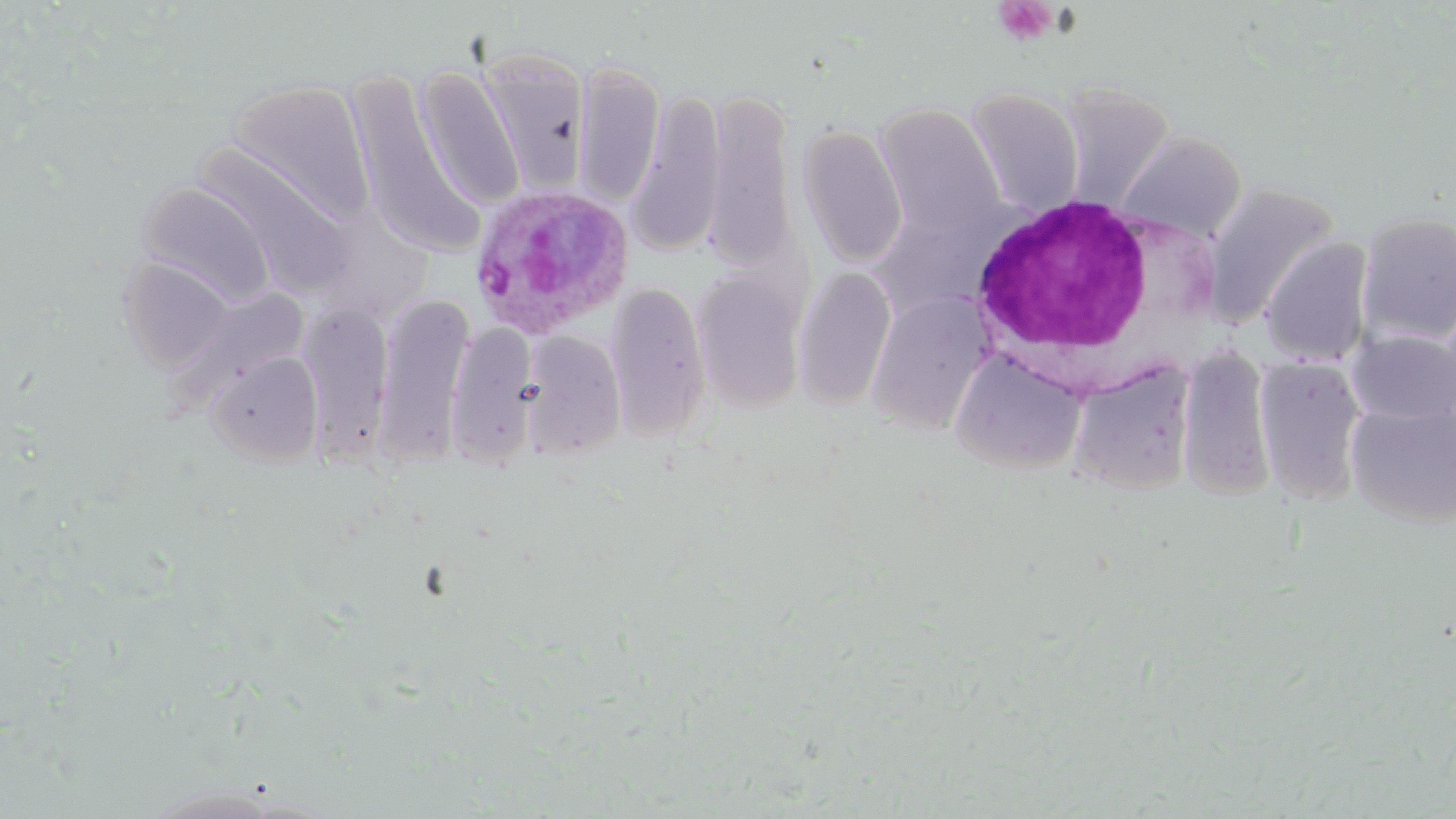
Summary:
  - Coordinate format: approximate bounding boxes as [x1, y1, x2, y2] in pixels
  - Platelet locations: [993, 1, 1057, 47]
  - White blood cell locations: [966, 193, 1165, 378]
  - Plasmodium ovale-infected red blood cell locations: [466, 183, 633, 341]
  - Uninfected red blood cell locations: [477, 48, 592, 194], [572, 60, 666, 207], [343, 66, 477, 257], [415, 66, 525, 210], [227, 78, 375, 227], [1057, 83, 1176, 211], [965, 87, 1086, 217], [627, 88, 726, 261], [705, 88, 799, 273], [873, 103, 1006, 242], [796, 123, 908, 269], [1117, 129, 1247, 243], [194, 144, 355, 299], [137, 182, 276, 307], [1201, 182, 1342, 328], [1357, 211, 1456, 346], [1260, 236, 1374, 367], [116, 257, 236, 372], [691, 266, 810, 412], [792, 267, 898, 409], [606, 281, 711, 441], [373, 292, 474, 468], [867, 292, 994, 435], [297, 300, 393, 465], [1435, 301, 1456, 429], [445, 321, 539, 469], [1346, 329, 1455, 425], [520, 331, 626, 460], [1176, 344, 1278, 500], [949, 348, 1087, 474], [206, 350, 324, 467], [1255, 356, 1367, 506], [1067, 360, 1197, 494], [1346, 401, 1456, 527]
  - Slide-level diagnosis: Plasmodium ovale
  - Modality: optical microscopy
  - Field of view: one of a larger specimen
  - Magnification: 1000x
  - Image size: 1456×819 pixels
  - Preparation: thin blood film
  - Stain: May-Grünwald-Giemsa